Locate every blood parasite and identify its species.
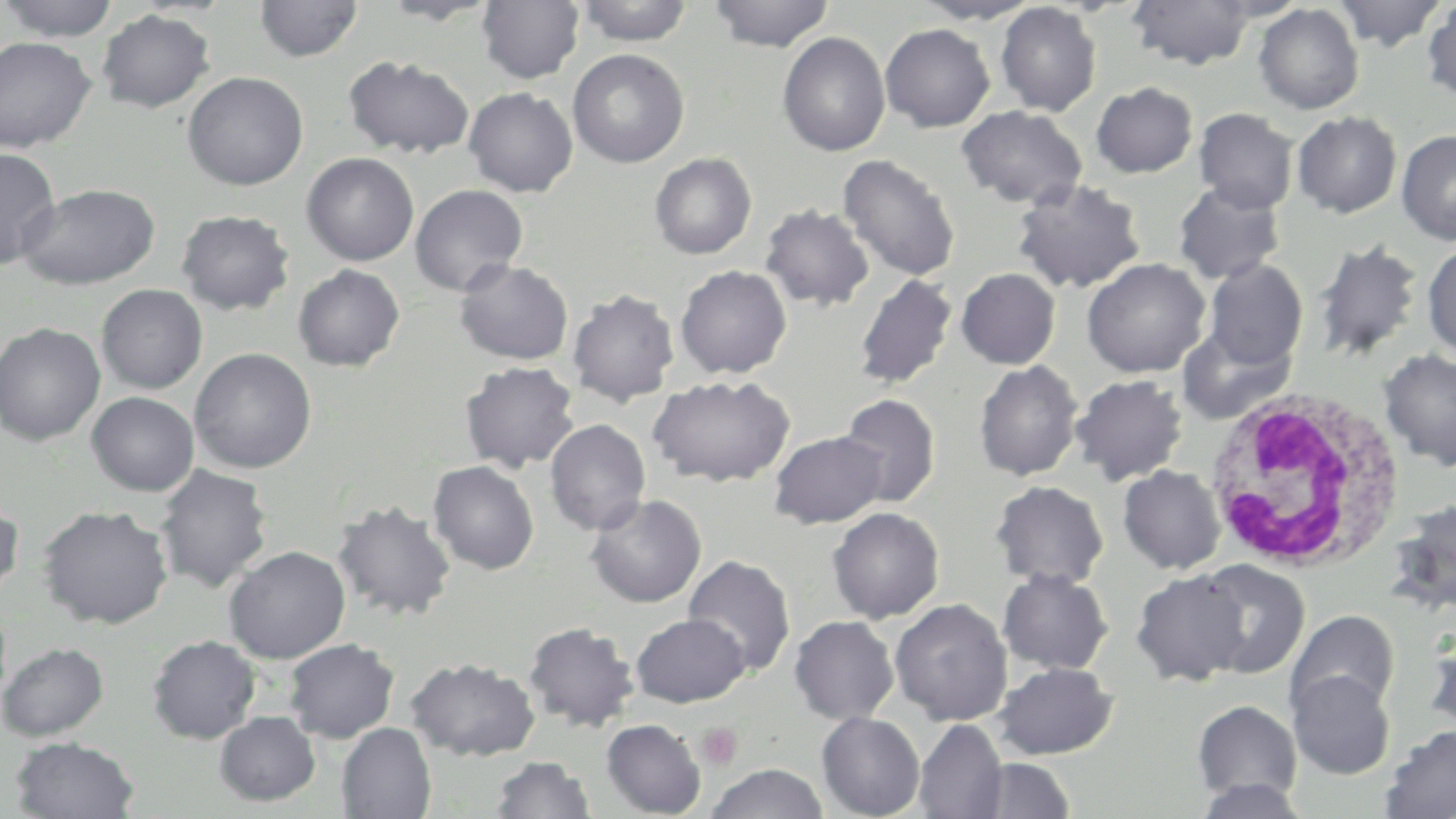

No blood parasites observed.

Approximate bounding boxes as named x1/y1/x2/y2 corners in pixels. Platelet locations: (x1=696, y1=722, x2=744, y2=771). White blood cell locations: (x1=1202, y1=388, x2=1406, y2=573). Uninfected red blood cell locations: (x1=255, y1=0, x2=363, y2=62), (x1=377, y1=0, x2=500, y2=23), (x1=575, y1=0, x2=694, y2=46), (x1=708, y1=0, x2=835, y2=52), (x1=1127, y1=0, x2=1257, y2=70), (x1=1199, y1=0, x2=1310, y2=22), (x1=1331, y1=0, x2=1450, y2=51), (x1=1421, y1=0, x2=1456, y2=105), (x1=2, y1=1, x2=119, y2=42), (x1=477, y1=1, x2=584, y2=84), (x1=914, y1=1, x2=1044, y2=25), (x1=995, y1=2, x2=1101, y2=116), (x1=1253, y1=3, x2=1364, y2=115), (x1=97, y1=9, x2=214, y2=112), (x1=880, y1=23, x2=995, y2=132), (x1=777, y1=31, x2=890, y2=157), (x1=0, y1=36, x2=97, y2=153), (x1=568, y1=49, x2=689, y2=168), (x1=343, y1=55, x2=475, y2=159), (x1=183, y1=71, x2=308, y2=190), (x1=1090, y1=82, x2=1198, y2=178), (x1=464, y1=87, x2=578, y2=197), (x1=957, y1=105, x2=1087, y2=210), (x1=1194, y1=108, x2=1298, y2=213), (x1=1292, y1=111, x2=1401, y2=218), (x1=1396, y1=129, x2=1456, y2=245), (x1=0, y1=147, x2=61, y2=268), (x1=301, y1=152, x2=419, y2=266), (x1=650, y1=152, x2=757, y2=259), (x1=838, y1=154, x2=961, y2=282), (x1=1011, y1=179, x2=1146, y2=294), (x1=1173, y1=181, x2=1285, y2=284), (x1=18, y1=183, x2=160, y2=289), (x1=409, y1=184, x2=528, y2=296), (x1=759, y1=203, x2=875, y2=312), (x1=176, y1=209, x2=295, y2=315), (x1=1312, y1=240, x2=1424, y2=363), (x1=1422, y1=241, x2=1456, y2=362), (x1=1082, y1=258, x2=1210, y2=378), (x1=455, y1=259, x2=574, y2=365), (x1=1203, y1=259, x2=1308, y2=370), (x1=293, y1=264, x2=405, y2=371), (x1=674, y1=265, x2=792, y2=379), (x1=956, y1=268, x2=1060, y2=369), (x1=854, y1=274, x2=957, y2=390), (x1=96, y1=284, x2=208, y2=394), (x1=567, y1=288, x2=679, y2=406), (x1=0, y1=322, x2=105, y2=446), (x1=1177, y1=325, x2=1295, y2=425), (x1=190, y1=348, x2=316, y2=473), (x1=1378, y1=349, x2=1456, y2=471), (x1=973, y1=360, x2=1083, y2=482), (x1=460, y1=361, x2=580, y2=473), (x1=648, y1=374, x2=796, y2=487), (x1=1071, y1=374, x2=1189, y2=486), (x1=86, y1=391, x2=199, y2=496), (x1=838, y1=394, x2=940, y2=509), (x1=544, y1=418, x2=651, y2=535), (x1=769, y1=430, x2=888, y2=529), (x1=428, y1=461, x2=540, y2=575), (x1=155, y1=464, x2=273, y2=593), (x1=1118, y1=465, x2=1225, y2=574), (x1=989, y1=480, x2=1109, y2=589), (x1=0, y1=494, x2=23, y2=602), (x1=584, y1=494, x2=707, y2=607), (x1=1390, y1=498, x2=1456, y2=616), (x1=332, y1=500, x2=456, y2=621), (x1=38, y1=505, x2=173, y2=629), (x1=827, y1=507, x2=945, y2=624), (x1=224, y1=545, x2=351, y2=663), (x1=682, y1=554, x2=796, y2=677), (x1=1194, y1=559, x2=1310, y2=679), (x1=997, y1=568, x2=1114, y2=675), (x1=1131, y1=569, x2=1250, y2=686), (x1=889, y1=598, x2=1013, y2=726), (x1=1286, y1=609, x2=1400, y2=718), (x1=631, y1=613, x2=749, y2=707), (x1=789, y1=615, x2=899, y2=725), (x1=523, y1=621, x2=639, y2=732), (x1=1422, y1=633, x2=1456, y2=736), (x1=148, y1=635, x2=261, y2=744), (x1=283, y1=638, x2=399, y2=743), (x1=0, y1=642, x2=109, y2=742), (x1=406, y1=657, x2=540, y2=761), (x1=993, y1=662, x2=1119, y2=760), (x1=1287, y1=670, x2=1395, y2=779), (x1=1192, y1=700, x2=1302, y2=804), (x1=214, y1=711, x2=320, y2=806), (x1=816, y1=712, x2=925, y2=819), (x1=601, y1=719, x2=706, y2=817), (x1=914, y1=719, x2=1008, y2=819), (x1=337, y1=723, x2=436, y2=819), (x1=1380, y1=725, x2=1456, y2=819), (x1=10, y1=736, x2=140, y2=818), (x1=489, y1=755, x2=595, y2=818), (x1=973, y1=757, x2=1075, y2=817), (x1=706, y1=763, x2=829, y2=818), (x1=1190, y1=778, x2=1312, y2=818). Slide-level diagnosis: negative for blood parasites. 1000x magnification. May-Grünwald-Giemsa-stained preparation. One field of a larger specimen. Image is 1456×819 pixels. Optical microscopy. Thin blood film.